Identify the parasite.
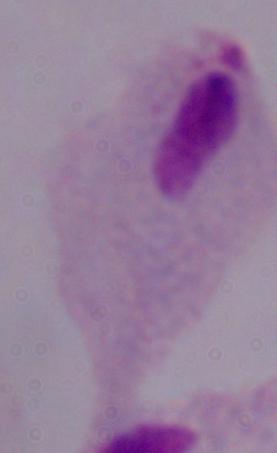
A trichomonad.

modality = micrograph
magnification = 1000x